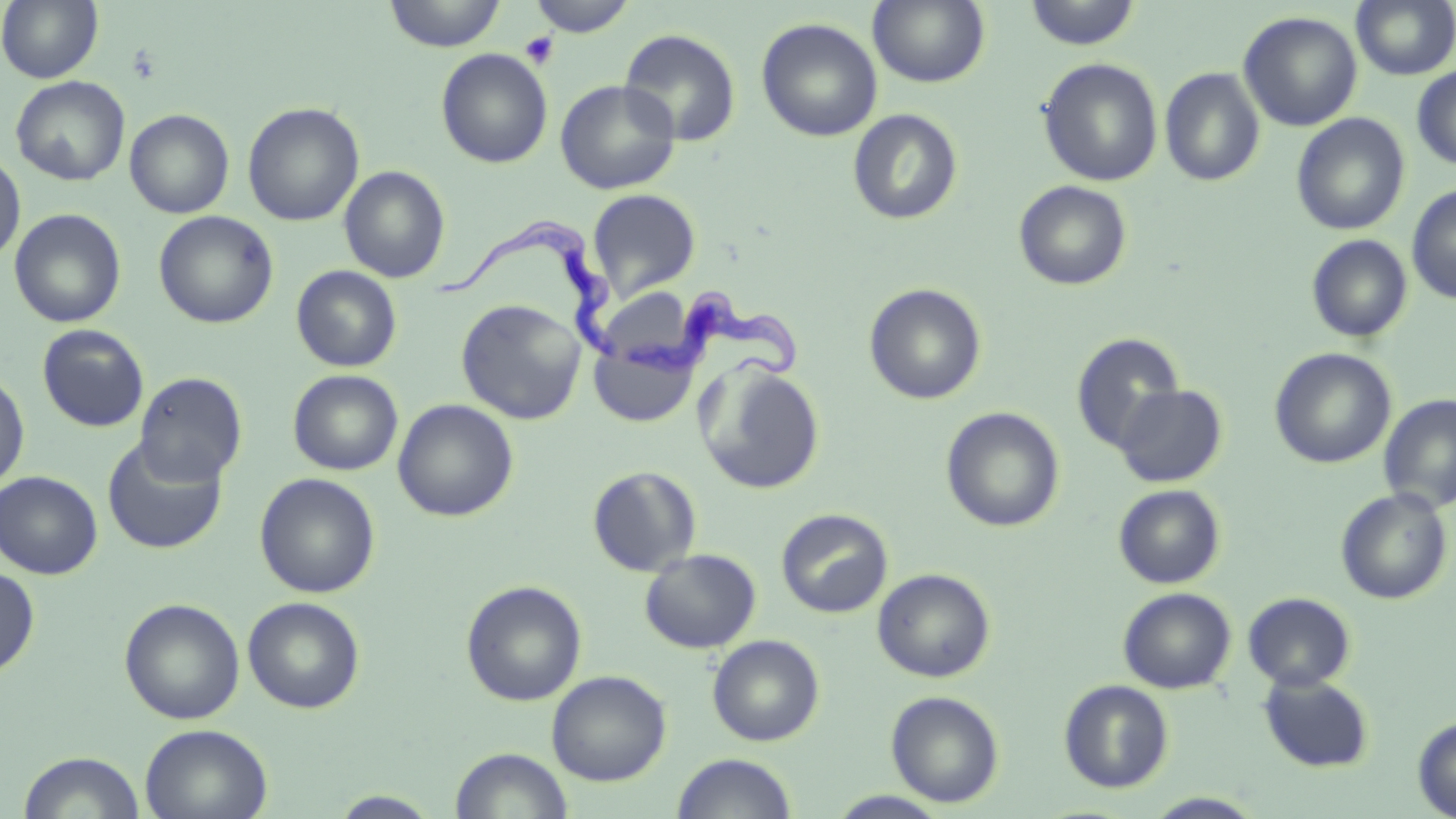

Summary:
  - Coordinate format: approximate bounding boxes as (x1, y1, x2, y2) in pixels
  - Trypanosoma brucei locations: (441, 209, 629, 368), (618, 293, 812, 390)
  - Platelet locations: (520, 32, 559, 70)
  - Uninfected red blood cell locations: (1, 0, 103, 83), (384, 0, 506, 52), (527, 0, 637, 37), (868, 0, 990, 89), (1351, 0, 1456, 81), (1023, 1, 1142, 50), (1238, 11, 1362, 132), (756, 17, 883, 143), (618, 28, 742, 147), (436, 48, 553, 168), (1038, 58, 1163, 186), (1412, 66, 1456, 172), (1159, 67, 1266, 187), (11, 75, 130, 186), (555, 79, 680, 195), (243, 102, 364, 226), (125, 109, 234, 218), (848, 109, 963, 226), (1291, 113, 1410, 235), (0, 150, 25, 266), (339, 165, 450, 283), (1013, 180, 1132, 290), (1406, 185, 1456, 304), (587, 189, 701, 302), (9, 208, 126, 328), (153, 210, 278, 328), (1306, 235, 1413, 343), (291, 265, 402, 371), (864, 283, 986, 405), (456, 298, 586, 425), (37, 324, 149, 432), (1070, 332, 1185, 455), (590, 342, 698, 427), (1270, 347, 1396, 469), (695, 362, 826, 495), (0, 366, 30, 491), (288, 369, 403, 475), (134, 372, 248, 486), (1113, 384, 1227, 487), (1378, 393, 1456, 514), (392, 398, 519, 522), (941, 407, 1065, 533), (101, 435, 229, 555), (587, 465, 702, 577), (0, 470, 103, 579), (255, 473, 380, 598), (1113, 484, 1226, 589), (1335, 488, 1453, 604), (776, 509, 893, 618), (640, 549, 761, 653), (0, 566, 40, 677), (872, 568, 995, 682), (461, 580, 587, 706), (1118, 587, 1236, 694), (1242, 591, 1356, 691), (242, 596, 365, 713), (119, 597, 246, 725), (707, 634, 825, 746), (546, 670, 672, 786), (1257, 674, 1374, 772), (1059, 679, 1173, 793), (886, 690, 1005, 808), (1412, 714, 1456, 818), (140, 723, 273, 819), (450, 747, 574, 818), (16, 750, 146, 819), (671, 752, 798, 818), (827, 790, 951, 818), (328, 791, 443, 818), (1142, 793, 1268, 818)
  - Slide-level diagnosis: Trypanosoma brucei
  - Preparation: thin blood smear
  - Stain: May-Grünwald-Giemsa
  - Modality: light microscopy
  - Magnification: 1000x
  - Image size: 1456×819 pixels
  - Field of view: single